Assess this cell for malaria.
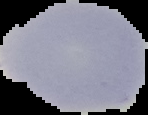
It is uninfected.

Summary:
  - Preparation: thin blood smear
  - Image size: 148×115 pixels
  - Image type: segmented cell region on a black background